Describe the morphology of the red blood cells.
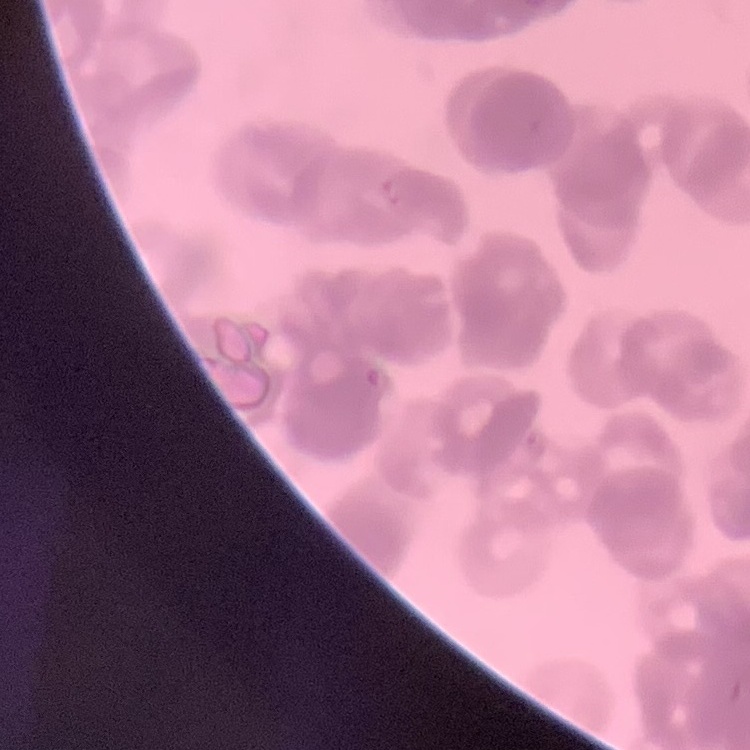
They show rouleaux formation.

stain = Field's or Giemsa
preparation = thin blood film
image type = one tile cut from a larger photomicrograph